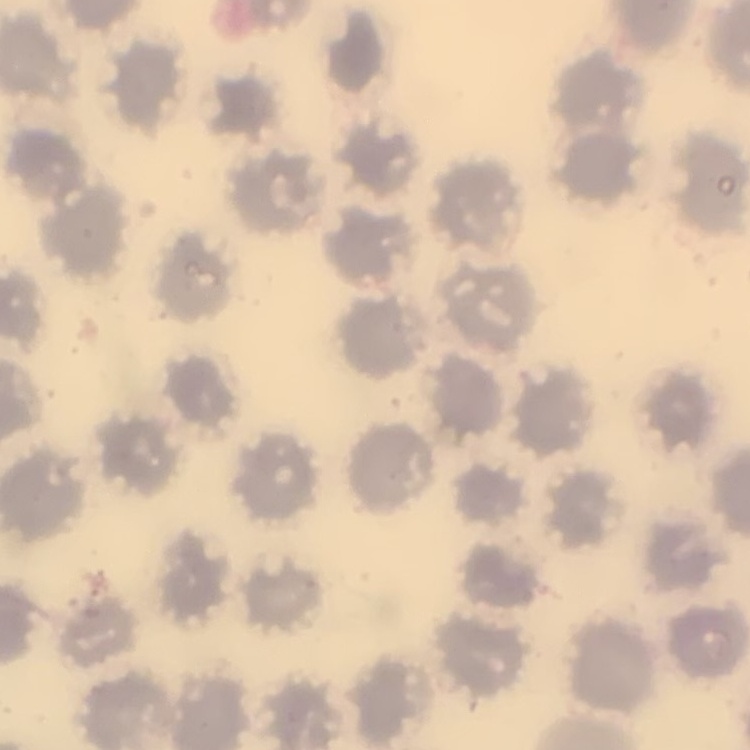

erythrocyte morphology = no rouleaux formation
stain = Field's or Giemsa
image type = square crop of a larger photomicrograph
preparation = thin blood film